Outline each blood parasite and name the species.
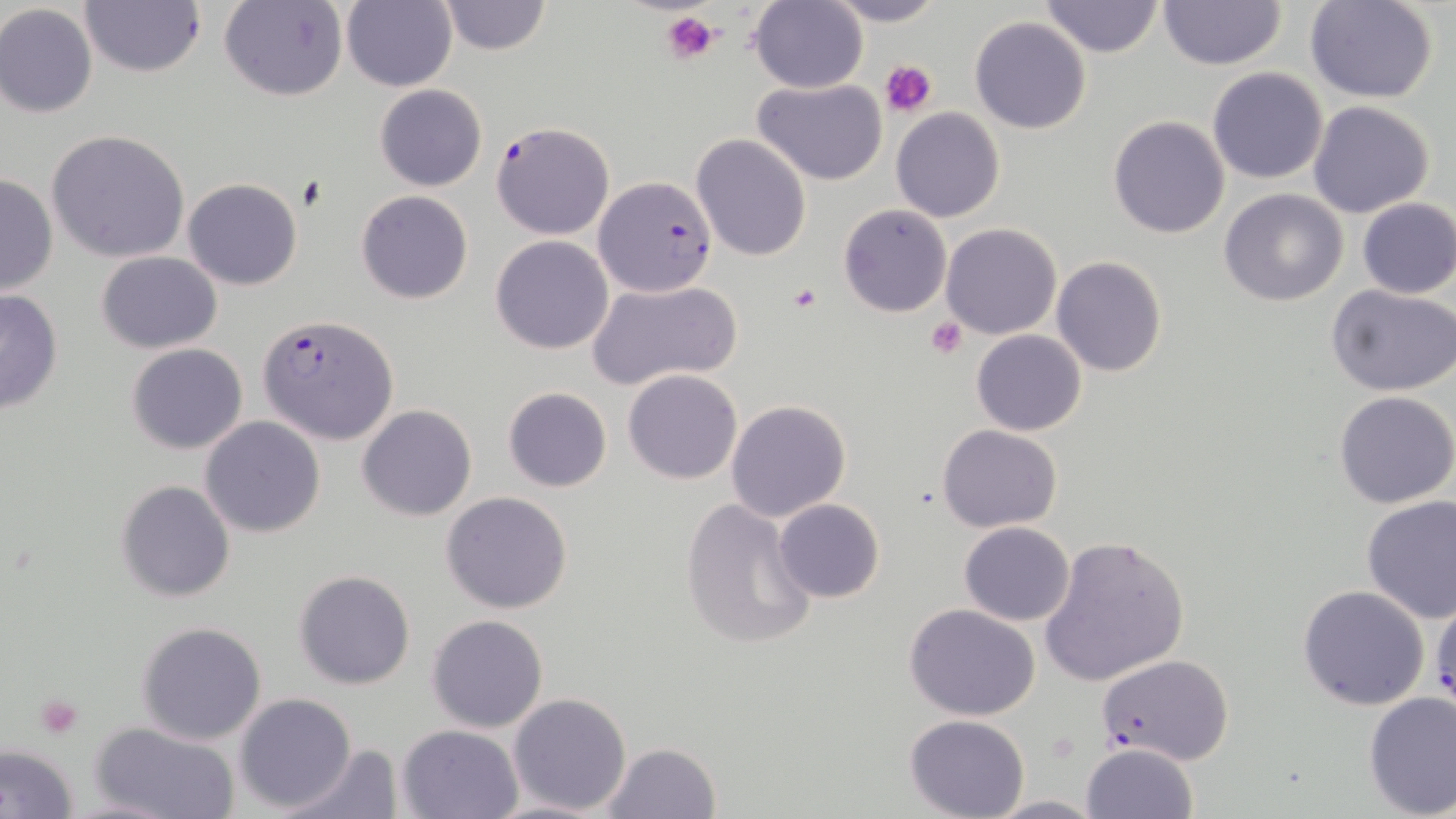

Approximate bounding boxes as named x1/y1/x2/y2 corners in pixels.
Plasmodium falciparum-infected red blood cells: (x1=490, y1=121, x2=615, y2=240), (x1=594, y1=177, x2=717, y2=296), (x1=256, y1=312, x2=401, y2=445), (x1=1095, y1=652, x2=1234, y2=767).
No Plasmodium ovale, Plasmodium malariae, Plasmodium vivax, Babesia divergens, or Trypanosoma brucei observed.

slide-level diagnosis = Plasmodium falciparum
field of view = single
stain = May-Grünwald-Giemsa
platelet locations = approximate bounding boxes as named x1/y1/x2/y2 corners in pixels: (x1=661, y1=10, x2=717, y2=66), (x1=880, y1=59, x2=938, y2=117), (x1=788, y1=283, x2=822, y2=312), (x1=927, y1=316, x2=969, y2=359), (x1=34, y1=693, x2=84, y2=738)
image size = 1456×819 pixels
modality = light microscopy
uninfected red blood cell locations = approximate bounding boxes as named x1/y1/x2/y2 corners in pixels: (x1=79, y1=0, x2=204, y2=77), (x1=436, y1=0, x2=551, y2=55), (x1=822, y1=0, x2=946, y2=27), (x1=1038, y1=0, x2=1165, y2=59), (x1=1304, y1=0, x2=1439, y2=103), (x1=219, y1=1, x2=348, y2=103), (x1=338, y1=1, x2=459, y2=89), (x1=749, y1=1, x2=869, y2=93), (x1=1158, y1=1, x2=1287, y2=71), (x1=0, y1=4, x2=98, y2=118), (x1=969, y1=16, x2=1092, y2=135), (x1=1207, y1=67, x2=1329, y2=184), (x1=753, y1=77, x2=888, y2=185), (x1=374, y1=84, x2=488, y2=192), (x1=1308, y1=100, x2=1435, y2=219), (x1=892, y1=109, x2=1005, y2=223), (x1=1108, y1=116, x2=1229, y2=239), (x1=46, y1=130, x2=191, y2=264), (x1=691, y1=133, x2=812, y2=261), (x1=0, y1=174, x2=58, y2=296), (x1=182, y1=177, x2=303, y2=290), (x1=1219, y1=189, x2=1349, y2=308), (x1=356, y1=191, x2=473, y2=305), (x1=1355, y1=197, x2=1456, y2=298), (x1=838, y1=204, x2=952, y2=317), (x1=940, y1=222, x2=1061, y2=341), (x1=489, y1=234, x2=616, y2=354), (x1=96, y1=251, x2=222, y2=353), (x1=1051, y1=255, x2=1168, y2=377), (x1=586, y1=278, x2=742, y2=391), (x1=1327, y1=285, x2=1456, y2=398), (x1=0, y1=288, x2=63, y2=415), (x1=971, y1=330, x2=1087, y2=436), (x1=126, y1=343, x2=248, y2=455), (x1=624, y1=368, x2=743, y2=484), (x1=503, y1=387, x2=612, y2=492), (x1=1333, y1=390, x2=1456, y2=510), (x1=725, y1=399, x2=851, y2=520), (x1=357, y1=404, x2=477, y2=521), (x1=200, y1=417, x2=326, y2=537), (x1=937, y1=423, x2=1063, y2=532), (x1=116, y1=480, x2=236, y2=602), (x1=440, y1=491, x2=572, y2=613), (x1=680, y1=497, x2=819, y2=651), (x1=1361, y1=497, x2=1456, y2=624), (x1=772, y1=498, x2=885, y2=604), (x1=959, y1=522, x2=1074, y2=625), (x1=1038, y1=533, x2=1190, y2=687), (x1=295, y1=568, x2=417, y2=690), (x1=1297, y1=584, x2=1431, y2=711), (x1=902, y1=603, x2=1041, y2=719), (x1=427, y1=614, x2=547, y2=733), (x1=136, y1=622, x2=268, y2=745), (x1=1362, y1=691, x2=1455, y2=817), (x1=233, y1=692, x2=357, y2=813), (x1=507, y1=693, x2=633, y2=814), (x1=904, y1=714, x2=1031, y2=819), (x1=91, y1=721, x2=242, y2=819), (x1=397, y1=724, x2=522, y2=818), (x1=0, y1=742, x2=79, y2=819), (x1=281, y1=742, x2=400, y2=819), (x1=600, y1=742, x2=725, y2=819), (x1=1080, y1=743, x2=1199, y2=819), (x1=987, y1=794, x2=1103, y2=817)
preparation = thin blood film
magnification = 1000x